Look for Plasmodium parasites.
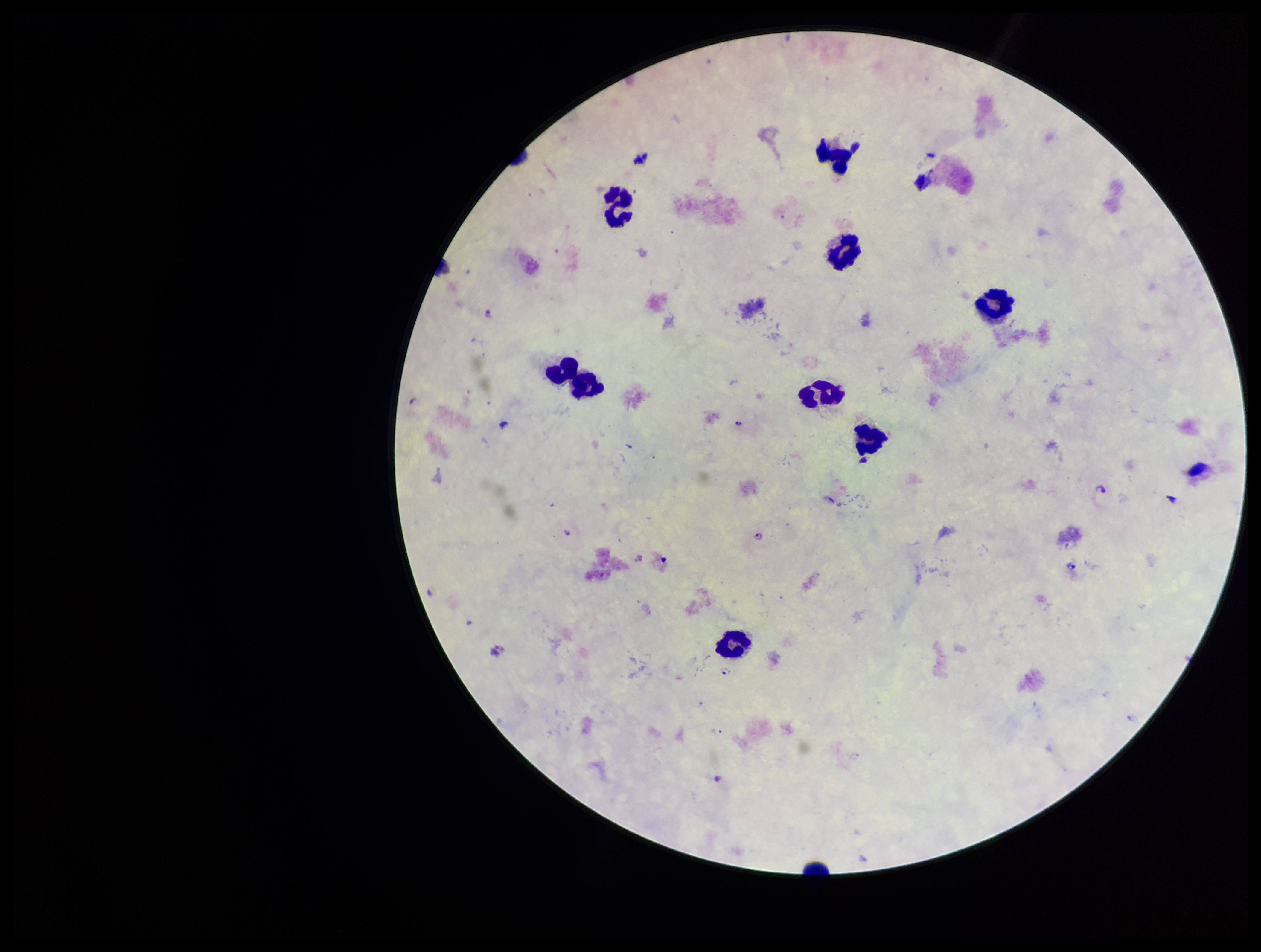
Seen.

parasite count = 3
image size = 1261×952 pixels
stain = Giemsa
field of view = one from this slide
leukocyte count = 10
patient malaria status = positive
capture = smartphone photograph through the microscope eyepiece
species reported for this patient = Plasmodium falciparum
preparation = thick blood smear